Describe the morphology of the erythrocytes.
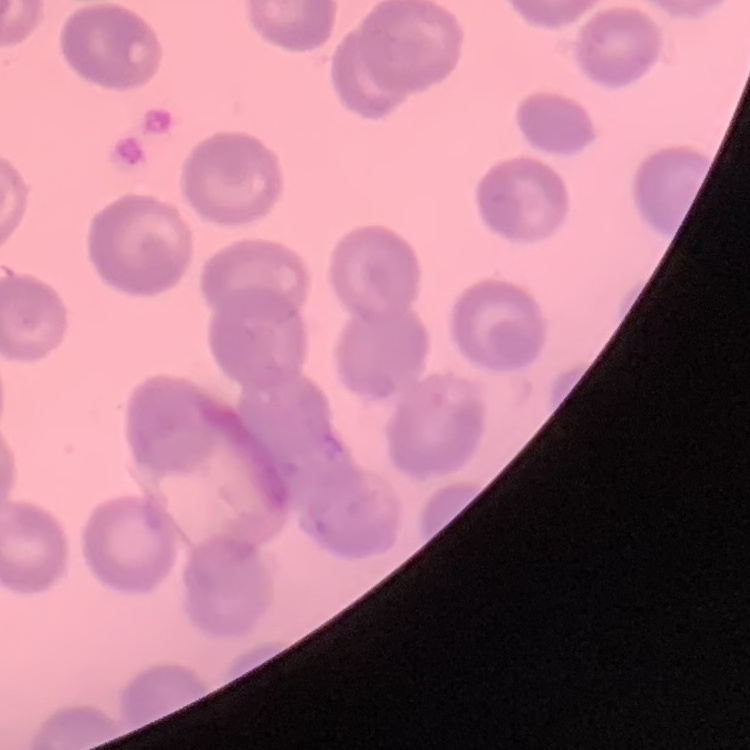
They show no rouleaux formation.

Summary:
  - Stain: Field's or Giemsa
  - Image type: one tile cut from a larger photomicrograph
  - Preparation: thin peripheral smear